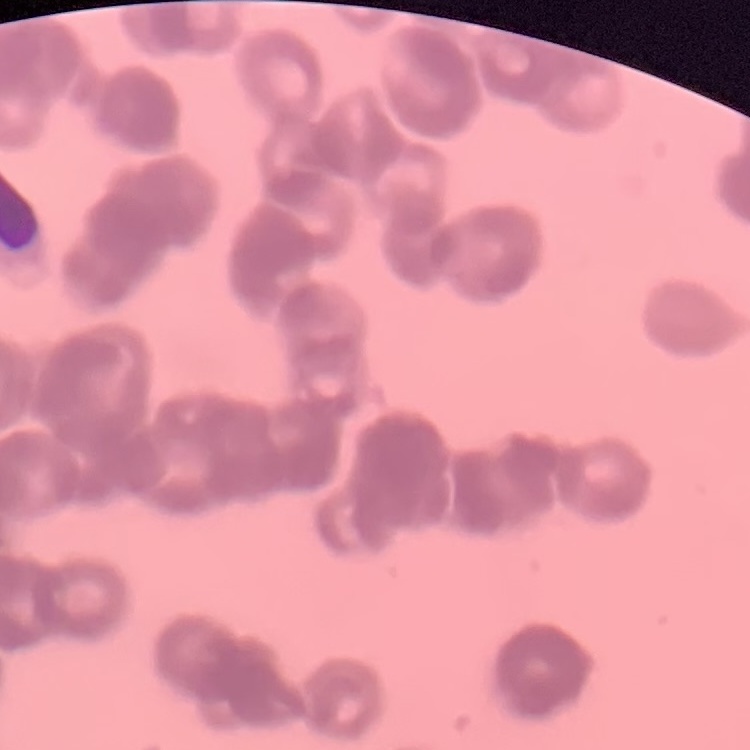 The red blood cells exhibit rouleaux formation. Stained with either Field's or Giemsa. Thin blood smear. One tile cut from a larger photomicrograph.